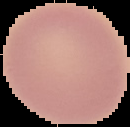

Summary:
  - Result: negative for Plasmodium parasites
  - Image size: 130×127 pixels
  - Image type: segmented cell region with the area outside set to black
  - Preparation: thin blood smear